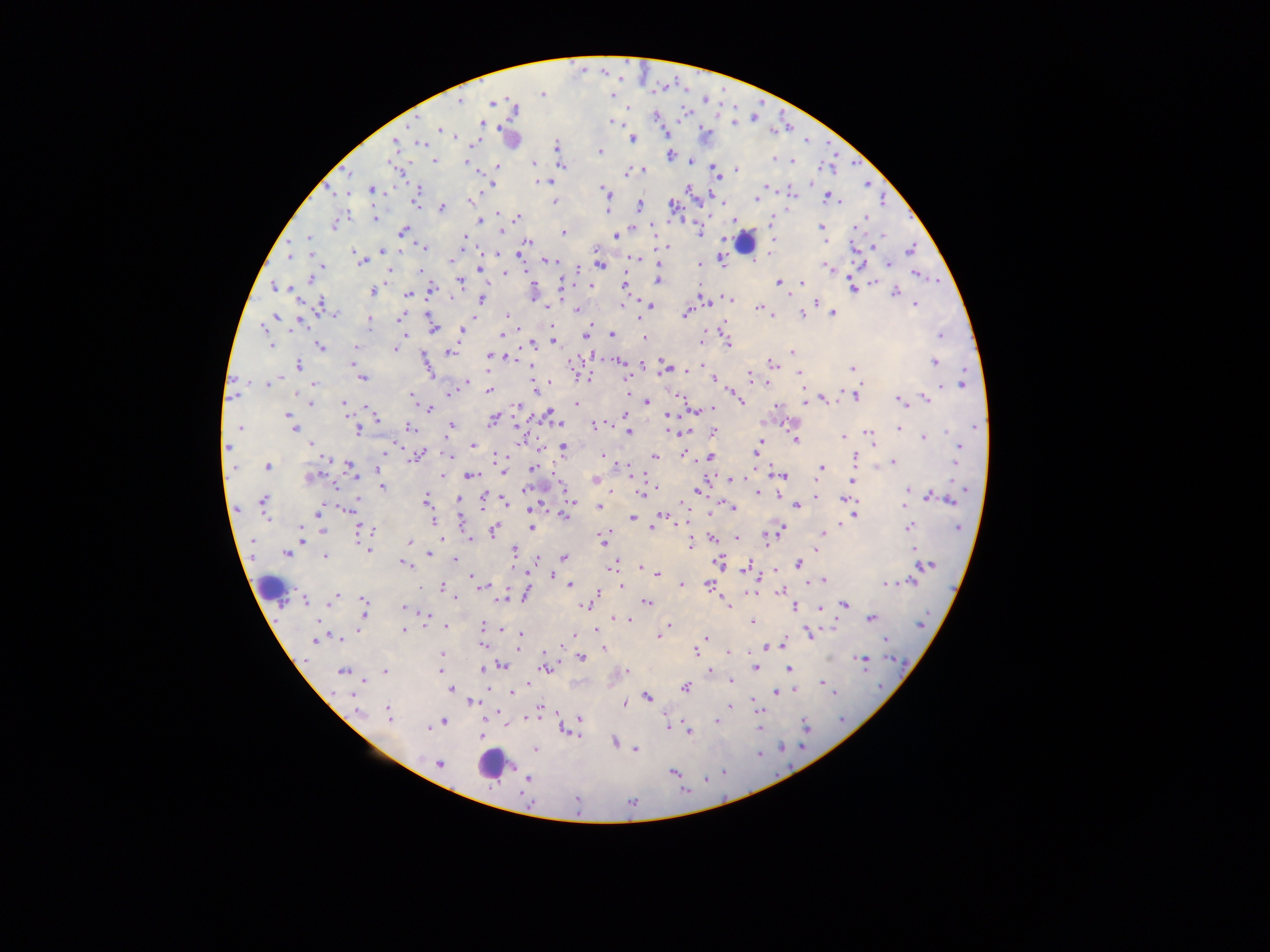

Approximate centers as {x, y} in pixels.
Summary:
  - Leukocyte locations: {743, 243}, {265, 586}, {490, 764}
  - Plasmodium parasite locations: {542, 93}, {460, 101}, {491, 103}, {515, 109}, {612, 121}, {481, 123}, {734, 123}, {439, 129}, {455, 137}, {633, 139}, {394, 142}, {421, 144}, {556, 146}, {601, 151}, {670, 155}, {774, 159}, {435, 160}, {791, 160}, {465, 161}, {691, 161}, {534, 163}, {498, 166}, {561, 166}, {643, 169}, {736, 169}, {627, 173}, {716, 176}, {538, 181}, {550, 181}, {493, 185}, {767, 186}, {688, 189}, {372, 190}, {419, 192}, {604, 192}, {792, 193}, {828, 198}, {756, 199}, {837, 200}, {470, 201}, {416, 202}, {554, 202}, {639, 205}, {673, 206}, {442, 207}, {607, 209}, {498, 213}, {517, 217}, {375, 218}, {734, 220}, {478, 221}, {771, 222}, {334, 224}, {822, 226}, {856, 226}, {403, 231}, {501, 232}, {563, 232}, {699, 233}, {615, 235}, {463, 236}, {309, 238}, {825, 239}, {772, 241}, {528, 242}, {423, 247}, {668, 247}, {382, 249}, {912, 249}, {353, 252}, {520, 254}, {288, 257}, {356, 257}, {637, 259}, {721, 259}, {451, 260}, {548, 260}, {362, 261}, {888, 263}, {699, 264}, {600, 265}, {578, 267}, {826, 267}, {481, 269}, {389, 271}, {420, 271}, {506, 272}, {526, 272}, {917, 275}, {310, 278}, {460, 281}, {657, 281}, {559, 283}, {778, 283}, {801, 283}, {624, 286}, {274, 287}, {590, 287}, {853, 288}, {432, 289}, {373, 291}, {894, 293}, {408, 295}, {451, 298}, {481, 299}, {730, 299}, {815, 302}, {707, 303}, {646, 304}, {321, 305}, {623, 305}, {650, 305}, {915, 305}, {544, 306}, {759, 307}, {577, 309}, {771, 313}, {833, 313}, {335, 314}, {685, 314}, {802, 314}, {506, 315}, {276, 316}, {400, 318}, {427, 319}, {640, 319}, {299, 321}, {369, 322}, {552, 326}, {590, 326}, {433, 328}, {462, 330}, {612, 334}, {584, 335}, {405, 336}, {502, 336}, {940, 336}, {552, 337}, {644, 338}, {553, 340}, {701, 342}, {532, 343}, {727, 344}, {271, 346}, {319, 346}, {356, 347}, {393, 349}, {450, 352}, {792, 352}, {487, 356}, {506, 358}, {354, 362}, {574, 362}, {619, 362}, {934, 362}, {641, 363}, {772, 365}, {299, 366}, {531, 367}, {666, 368}, {852, 368}, {688, 370}, {799, 374}, {749, 376}, {362, 377}, {588, 378}, {713, 378}, {467, 382}, {767, 382}, {267, 384}, {315, 384}, {942, 385}, {962, 385}, {489, 390}, {534, 390}, {297, 394}, {449, 394}, {233, 395}, {410, 395}, {737, 397}, {855, 397}, {925, 398}, {825, 399}, {899, 399}, {741, 400}, {805, 401}, {809, 401}, {311, 403}, {344, 403}, {648, 403}, {576, 404}, {517, 406}, {777, 406}, {712, 409}, {429, 410}, {549, 415}, {625, 415}, {671, 415}, {289, 416}, {493, 419}, {378, 420}, {451, 426}, {595, 426}, {410, 427}, {240, 428}, {293, 429}, {899, 429}, {358, 430}, {671, 431}, {629, 432}, {713, 432}, {868, 432}, {683, 433}, {869, 436}, {843, 437}, {923, 438}, {761, 441}, {796, 441}, {311, 444}, {473, 445}, {393, 446}, {759, 446}, {229, 447}, {563, 448}, {757, 449}, {958, 451}, {385, 454}, {684, 454}, {497, 455}, {420, 456}, {448, 456}, {603, 456}, {654, 457}, {712, 457}, {854, 457}, {326, 459}, {957, 459}, {893, 462}, {267, 466}, {350, 466}, {233, 467}, {822, 468}, {532, 469}, {378, 470}, {502, 471}, {355, 476}, {440, 476}, {470, 476}, {783, 476}, {309, 478}, {732, 479}, {737, 479}, {594, 480}, {853, 481}, {382, 487}, {524, 489}, {697, 491}, {908, 491}, {758, 493}, {640, 495}, {816, 496}, {929, 496}, {458, 498}, {483, 499}, {425, 500}, {846, 500}, {950, 500}, {263, 501}, {571, 501}, {506, 503}, {796, 505}, {904, 505}, {599, 507}, {733, 508}, {347, 509}, {318, 512}, {711, 514}, {855, 515}, {564, 516}, {662, 517}, {632, 518}, {461, 520}, {433, 521}, {530, 527}, {909, 527}, {958, 527}, {653, 529}, {781, 529}, {301, 530}, {321, 530}, {362, 530}, {493, 531}, {823, 533}, {605, 536}, {737, 537}, {711, 538}, {470, 539}, {303, 540}, {603, 540}, {766, 540}, {409, 543}, {690, 545}, {367, 549}, {914, 549}, {514, 550}, {286, 553}, {429, 553}, {325, 556}, {564, 557}, {537, 558}, {455, 560}, {718, 561}, {799, 563}, {405, 564}, {614, 565}, {926, 565}, {746, 567}, {641, 569}, {657, 573}, {551, 575}, {472, 577}, {824, 580}, {911, 581}, {708, 584}, {886, 584}, {569, 585}, {681, 585}, {483, 586}, {621, 586}, {442, 587}, {420, 588}, {598, 591}, {780, 592}, {525, 594}, {336, 596}, {454, 597}, {304, 600}, {502, 600}, {364, 601}, {330, 602}, {647, 602}, {728, 605}, {845, 605}, {586, 606}, {403, 607}, {795, 607}, {820, 609}, {364, 612}, {427, 615}, {614, 618}, {870, 619}, {628, 620}, {752, 621}, {921, 625}, {483, 626}, {667, 626}, {446, 627}, {502, 629}, {405, 631}, {809, 632}, {574, 635}, {520, 636}, {659, 636}, {705, 638}, {340, 639}, {316, 640}, {885, 640}, {780, 644}, {483, 645}, {768, 647}, {603, 649}, {695, 652}, {729, 652}, {442, 655}, {581, 657}, {861, 660}, {503, 665}, {545, 667}, {756, 667}, {790, 668}, {483, 669}, {343, 671}, {440, 671}, {626, 671}, {385, 672}, {710, 672}, {732, 681}, {822, 683}, {528, 684}, {826, 686}, {685, 688}, {451, 689}, {794, 690}, {512, 692}, {776, 692}, {352, 693}, {648, 697}, {752, 702}, {473, 703}, {624, 703}, {729, 707}, {757, 707}, {540, 709}, {358, 712}, {498, 712}, {388, 713}, {532, 717}, {580, 719}, {716, 721}, {444, 722}, {435, 725}, {668, 726}, {806, 726}, {428, 728}, {759, 728}, {688, 732}, {481, 737}, {614, 742}, {635, 749}, {535, 750}, {439, 764}, {673, 772}, {528, 778}, {576, 801}
  - Field of view: single
  - Image size: 1270×952 pixels
  - Capture: mobile-phone photograph through a microscope
  - Country: Ghana
  - Preparation: thick blood film